Name the parasite shown.
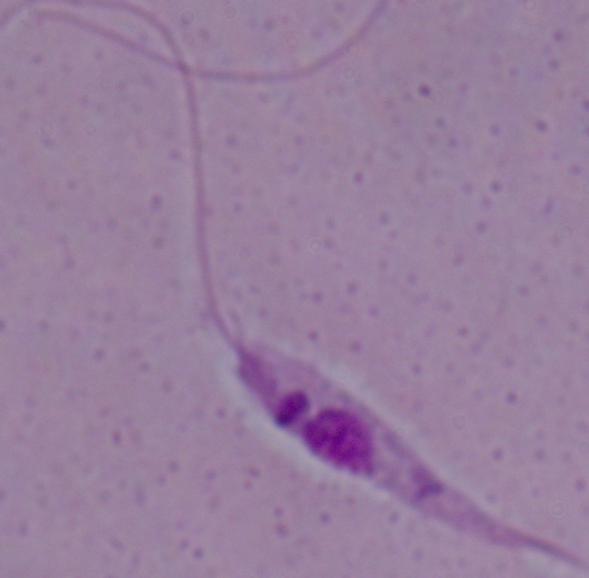

This is Leishmania.

Photomicrograph. Captured at 1000x magnification.